Report the malaria status of this cell.
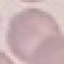

Uninfected.

Thin smear of blood. Cell patch, automatically extracted from a larger field of view and resized to 64 × 64 pixels. Giemsa-stained preparation. Photographed with a smartphone camera at the microscope eyepiece.